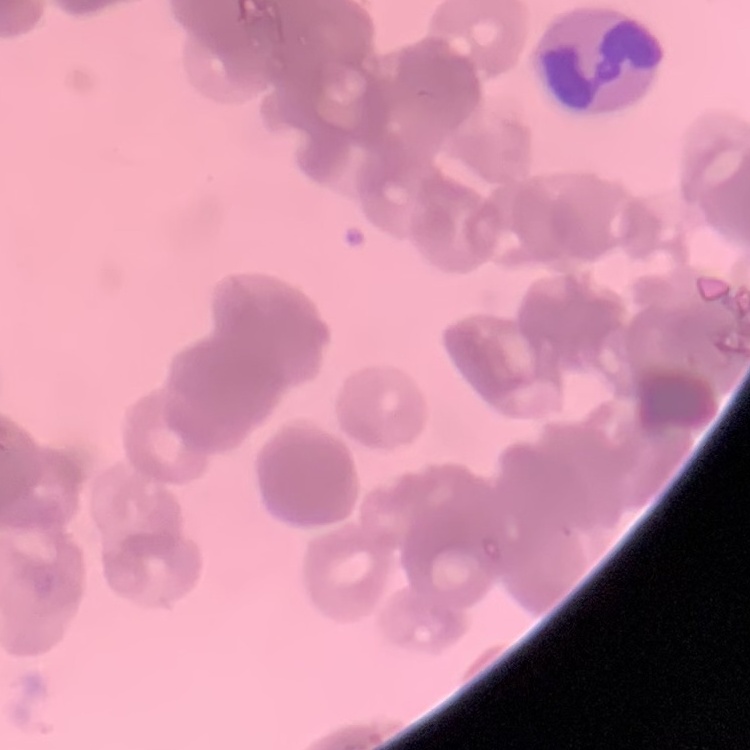

Summary:
  - Erythrocyte morphology: rouleaux formation
  - Stain: Field's or Giemsa
  - Preparation: thin blood smear
  - Image type: one tile cut from a larger photomicrograph